Name the parasite shown.
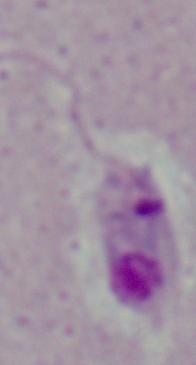
This is Leishmania.

Photomicrograph. Captured at 1000x magnification.